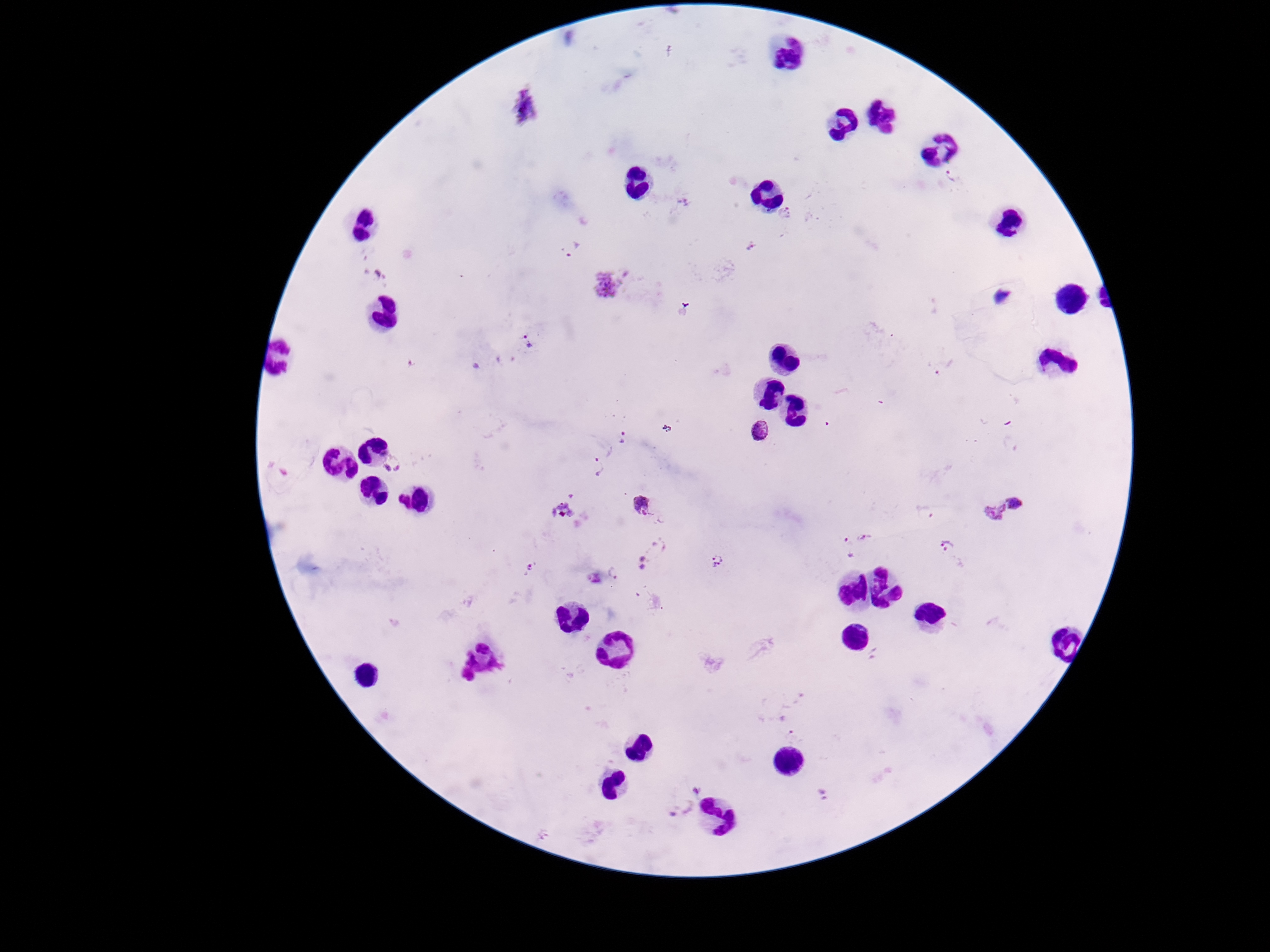
Approximate centers as [x, y] in pixels. Plasmodium parasite locations: [954, 175], [684, 201], [787, 214], [751, 246], [572, 247], [608, 285], [529, 342], [944, 369], [759, 430], [623, 438], [394, 466], [594, 467], [1018, 503], [641, 505], [924, 513], [994, 513], [866, 538], [947, 545], [847, 547], [652, 554], [718, 562], [531, 569], [616, 575], [595, 577], [698, 789], [824, 793], [678, 809]. Patient malaria status: positive. 100x magnification. Giemsa stain. Thick blood smear. Image is 1270×952 pixels. Single field of view. Smartphone photograph taken through the microscope eyepiece.